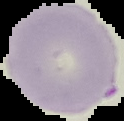

Summary:
  - Image type: segmented cell region with the area outside set to black
  - Image size: 124×121 pixels
  - Result: no Plasmodium parasites seen
  - Preparation: thin blood film